Assess for malaria.
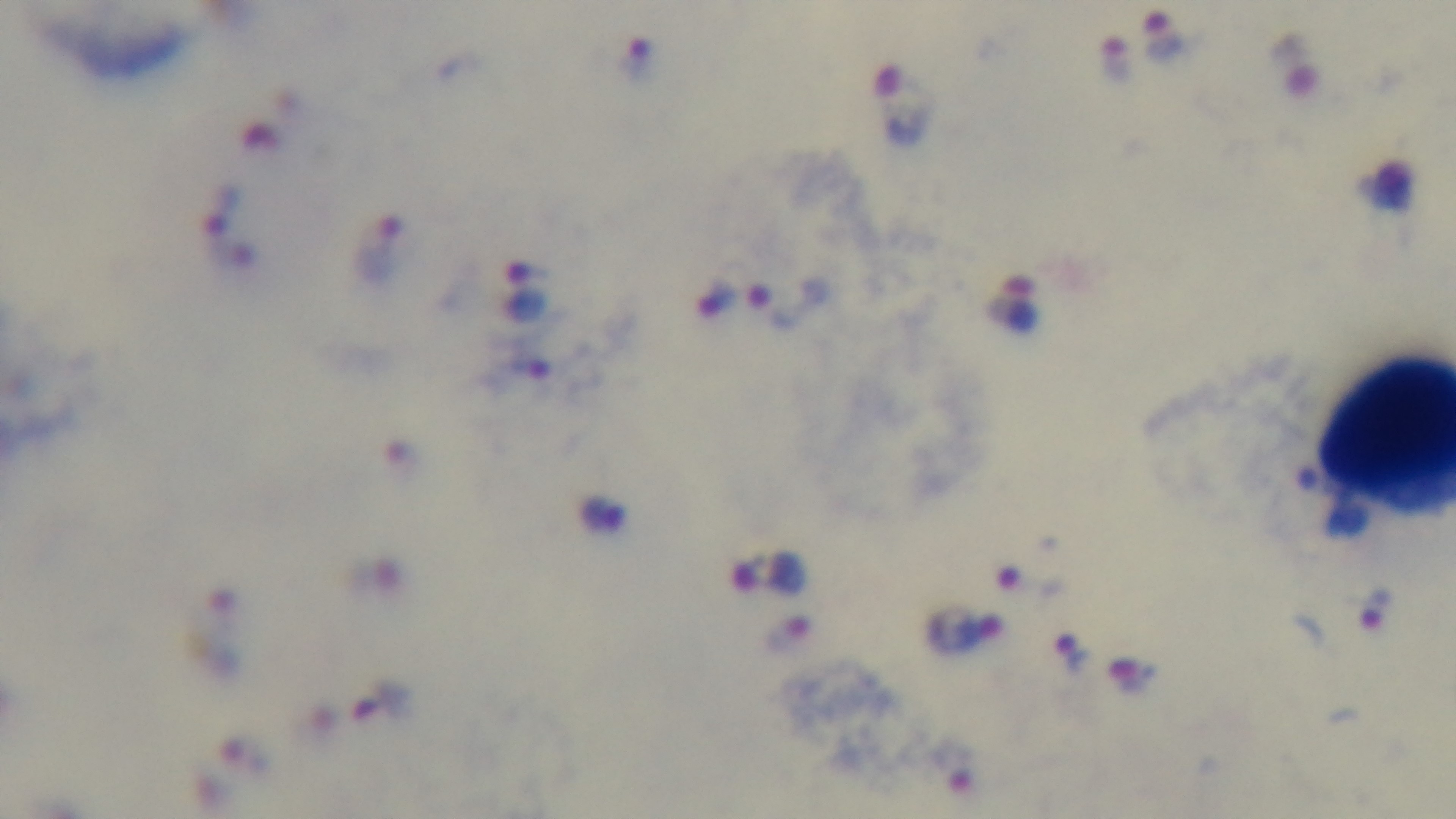
Positive.

One field from the slide. Mounted 4K digital camera. Photomicrograph. Preparation: thick smear. 100x oil-immersion objective. Giemsa stain.